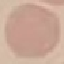

Summary:
  - Result: no malaria parasites seen
  - Preparation: thin smear
  - Stain: Giemsa
  - Image type: automatically extracted cell patch, resized to 64 × 64 pixels
  - Capture: smartphone through the microscope eyepiece